State which parasite is depicted.
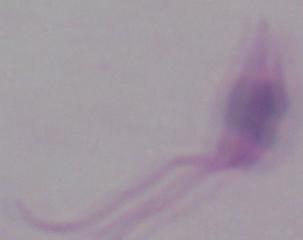

This is Leishmania.

magnification = 1000x
modality = photomicrograph